Outline platelets.
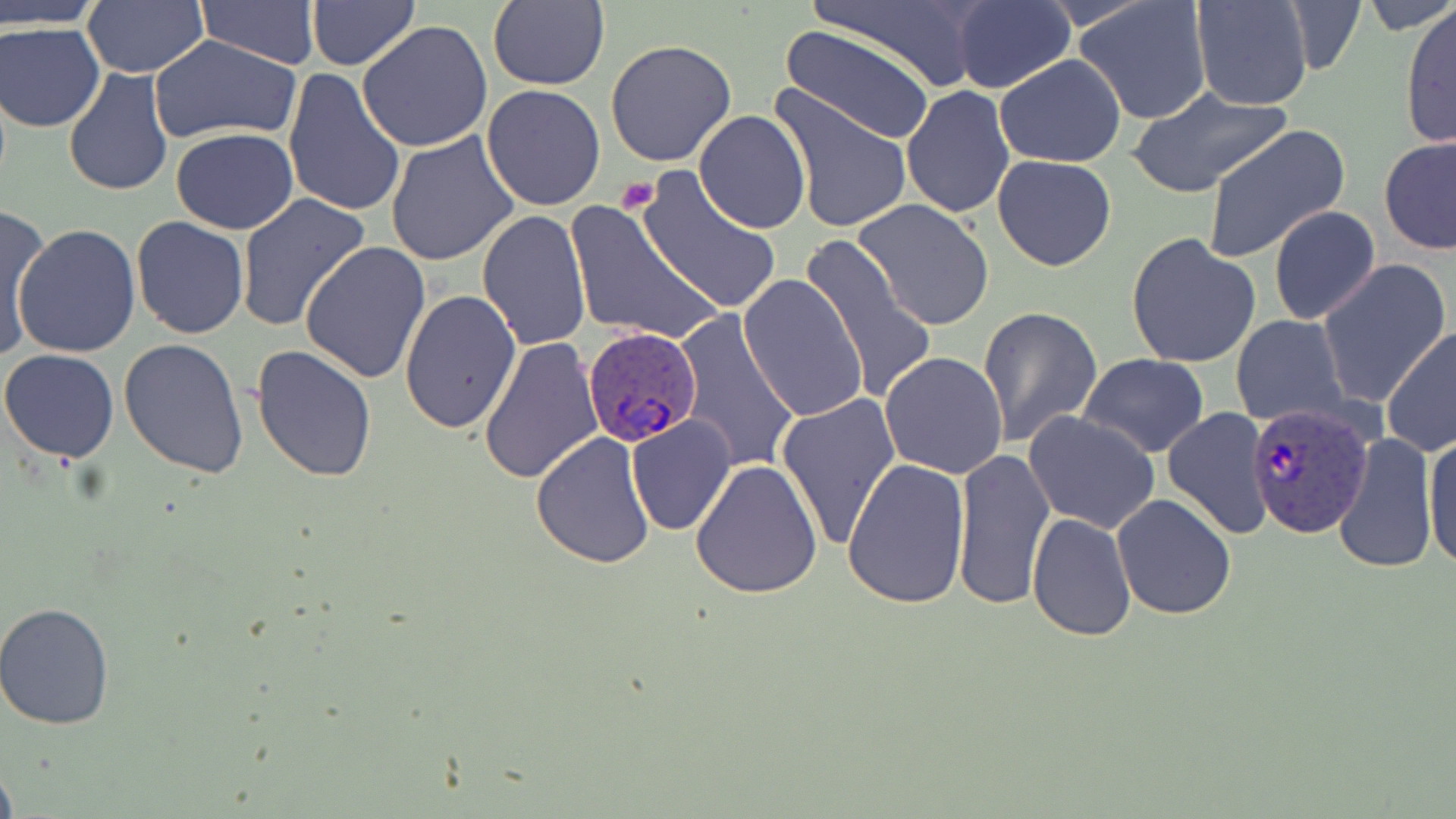
Approximate bounding boxes as named x1/y1/x2/y2 corners in pixels.
Platelets: (x1=616, y1=178, x2=659, y2=213).

{
  "slide_level_diagnosis": "Plasmodium ovale",
  "image_size": "1456×819 pixels",
  "plasmodium_ovale_infected_red_blood_cell_locations": "approximate bounding boxes as named x1/y1/x2/y2 corners in pixels: (x1=581, y1=325, x2=706, y2=450), (x1=1245, y1=402, x2=1376, y2=542)",
  "preparation": "thin blood smear",
  "stain": "May-Grünwald-Giemsa",
  "uninfected_red_blood_cell_locations": "approximate bounding boxes as named x1/y1/x2/y2 corners in pixels: (x1=196, y1=0, x2=322, y2=68), (x1=807, y1=0, x2=988, y2=94), (x1=950, y1=0, x2=1077, y2=95), (x1=1073, y1=0, x2=1213, y2=126), (x1=1190, y1=0, x2=1312, y2=110), (x1=1283, y1=0, x2=1368, y2=76), (x1=1360, y1=0, x2=1453, y2=35), (x1=1, y1=1, x2=106, y2=27), (x1=81, y1=1, x2=208, y2=79), (x1=305, y1=1, x2=418, y2=70), (x1=487, y1=1, x2=610, y2=90), (x1=1399, y1=3, x2=1455, y2=151), (x1=357, y1=21, x2=493, y2=153), (x1=1, y1=22, x2=106, y2=132), (x1=1021, y1=25, x2=1185, y2=155), (x1=781, y1=27, x2=937, y2=146), (x1=148, y1=34, x2=300, y2=146), (x1=605, y1=39, x2=737, y2=170), (x1=994, y1=54, x2=1127, y2=168), (x1=62, y1=68, x2=175, y2=194), (x1=283, y1=68, x2=406, y2=220), (x1=480, y1=84, x2=606, y2=212), (x1=765, y1=84, x2=914, y2=235), (x1=900, y1=85, x2=1015, y2=216), (x1=1125, y1=88, x2=1294, y2=200), (x1=694, y1=110, x2=811, y2=232), (x1=1202, y1=124, x2=1352, y2=264), (x1=171, y1=129, x2=298, y2=234), (x1=385, y1=132, x2=520, y2=268), (x1=1379, y1=136, x2=1456, y2=256), (x1=991, y1=154, x2=1118, y2=272), (x1=635, y1=167, x2=782, y2=315), (x1=237, y1=194, x2=370, y2=333), (x1=850, y1=198, x2=996, y2=332), (x1=565, y1=200, x2=720, y2=347), (x1=1267, y1=204, x2=1380, y2=326), (x1=2, y1=206, x2=50, y2=360), (x1=476, y1=210, x2=593, y2=350), (x1=131, y1=216, x2=249, y2=338), (x1=13, y1=224, x2=142, y2=360), (x1=1125, y1=232, x2=1263, y2=370), (x1=797, y1=234, x2=942, y2=403), (x1=300, y1=240, x2=432, y2=383), (x1=1316, y1=258, x2=1452, y2=409), (x1=738, y1=273, x2=869, y2=422), (x1=400, y1=289, x2=521, y2=436), (x1=977, y1=305, x2=1104, y2=447), (x1=675, y1=312, x2=798, y2=475), (x1=1230, y1=315, x2=1349, y2=426), (x1=1382, y1=326, x2=1456, y2=456), (x1=478, y1=336, x2=604, y2=485), (x1=118, y1=339, x2=248, y2=478), (x1=251, y1=345, x2=377, y2=483), (x1=0, y1=348, x2=121, y2=463), (x1=878, y1=351, x2=1009, y2=480), (x1=1077, y1=353, x2=1208, y2=457), (x1=775, y1=393, x2=900, y2=551), (x1=1162, y1=407, x2=1274, y2=540), (x1=1023, y1=410, x2=1162, y2=534), (x1=625, y1=415, x2=736, y2=537), (x1=531, y1=432, x2=656, y2=569), (x1=1423, y1=432, x2=1456, y2=573), (x1=1331, y1=433, x2=1439, y2=573), (x1=950, y1=447, x2=1055, y2=611), (x1=840, y1=456, x2=969, y2=611), (x1=689, y1=457, x2=824, y2=599), (x1=1112, y1=494, x2=1237, y2=621), (x1=1027, y1=514, x2=1138, y2=642), (x1=0, y1=602, x2=116, y2=731), (x1=0, y1=754, x2=19, y2=819)",
  "modality": "optical microscopy",
  "field_of_view": "one of a larger specimen",
  "magnification": "1000x"
}